Report the malaria status of this cell.
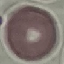
Uninfected.

Acquired by smartphone through the microscope eyepiece. Automatically extracted cell patch, resized to 64 × 64 pixels. Thin smear of blood. Giemsa-stained preparation.